Classify this cell by malaria status.
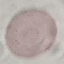

It is uninfected.

capture = smartphone camera at the microscope eyepiece
preparation = thin blood film
image type = automatically extracted cell patch, resized to 64 × 64 pixels
stain = Giemsa